Classify this cell by malaria status.
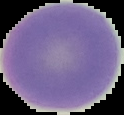
It is uninfected.

Image is 124×115 pixels. The area outside the segmented cell region is set to black. From a thin blood film.